Report the malaria status of this cell.
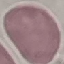
It is uninfected.

Giemsa-stained preparation. Cell patch, automatically extracted from a larger field of view and resized to 64 × 64 pixels. Photographed with a smartphone camera at the microscope eyepiece. Thin smear of blood.